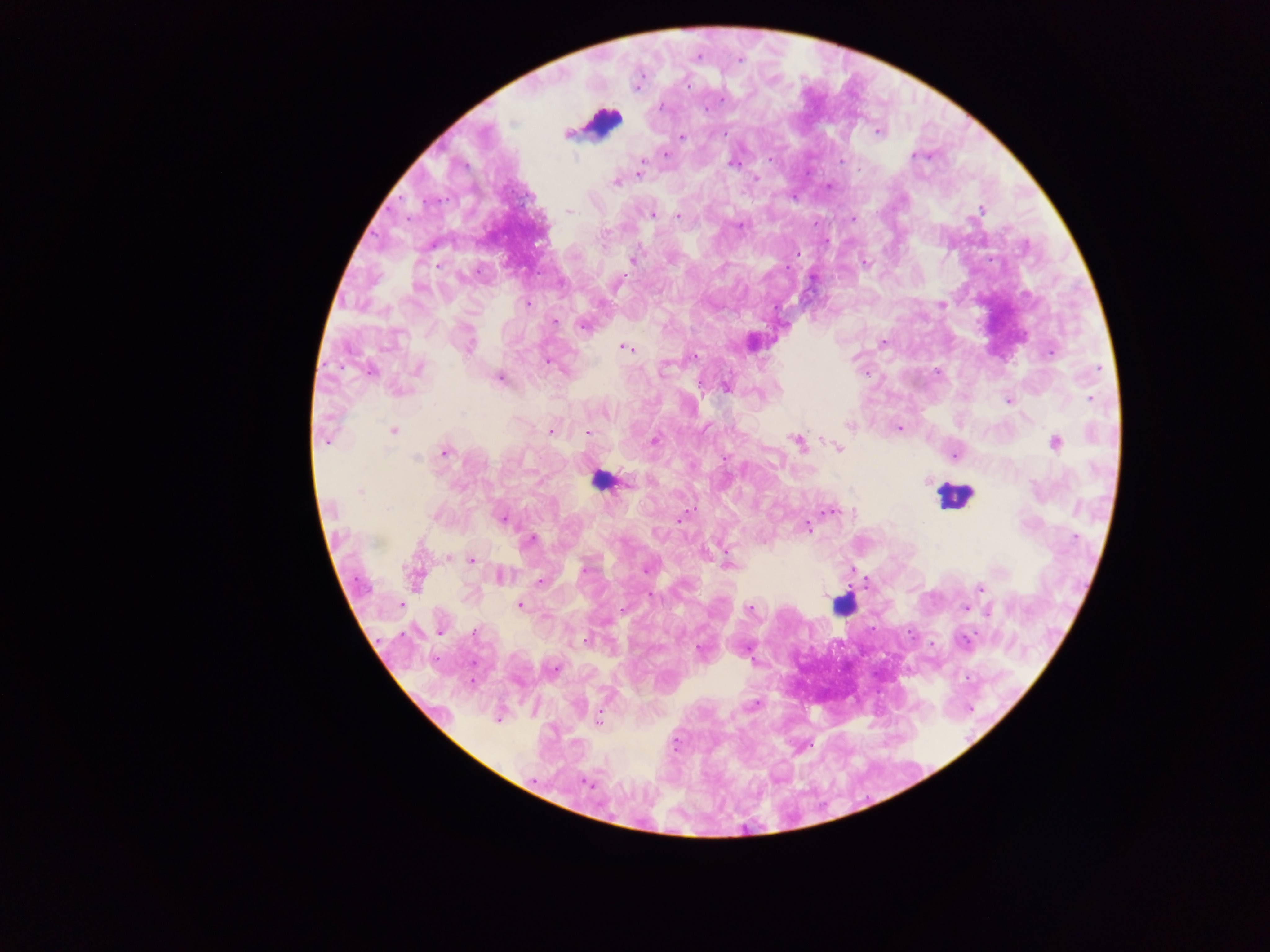

image size = 1270×952 pixels
field of view = single
leukocyte locations = approximate centers as (x, y) in pixels: (603, 121), (598, 480), (954, 496), (842, 606)
country = Ghana
malaria parasite locations = approximate centers as (x, y) in pixels: (698, 57), (740, 60), (688, 85), (721, 100), (661, 106), (566, 133), (725, 133), (878, 133), (681, 137), (665, 154), (913, 156), (770, 159), (642, 161), (841, 161), (732, 164), (859, 168), (639, 174), (756, 178), (616, 182), (828, 186), (981, 210), (569, 212), (652, 214), (677, 216), (852, 219), (740, 225), (632, 260), (866, 262), (527, 304), (942, 304), (555, 321), (582, 326), (883, 342), (469, 347), (627, 348), (1051, 353), (693, 357), (547, 362), (418, 369), (370, 371), (500, 378), (726, 387), (400, 391), (1091, 398), (1008, 401), (849, 425), (900, 428), (393, 430), (550, 431), (588, 433), (326, 441), (655, 441), (797, 442), (1055, 442), (838, 448), (444, 452), (955, 456), (417, 458), (627, 482), (927, 482), (359, 492), (387, 508), (832, 511), (435, 516), (681, 517), (503, 519), (808, 527), (1076, 538), (531, 540), (448, 558), (472, 560), (727, 563), (585, 570), (646, 571), (503, 576), (540, 581), (980, 587), (651, 596), (401, 604), (520, 605), (966, 608), (750, 609), (989, 612), (472, 631), (439, 632), (585, 640), (964, 642), (699, 650), (554, 668), (472, 681), (754, 705), (498, 720), (598, 720), (676, 743), (586, 783)
capture = mobile-phone photograph through a microscope
preparation = thick blood smear